Locate every blood parasite and identify its species.
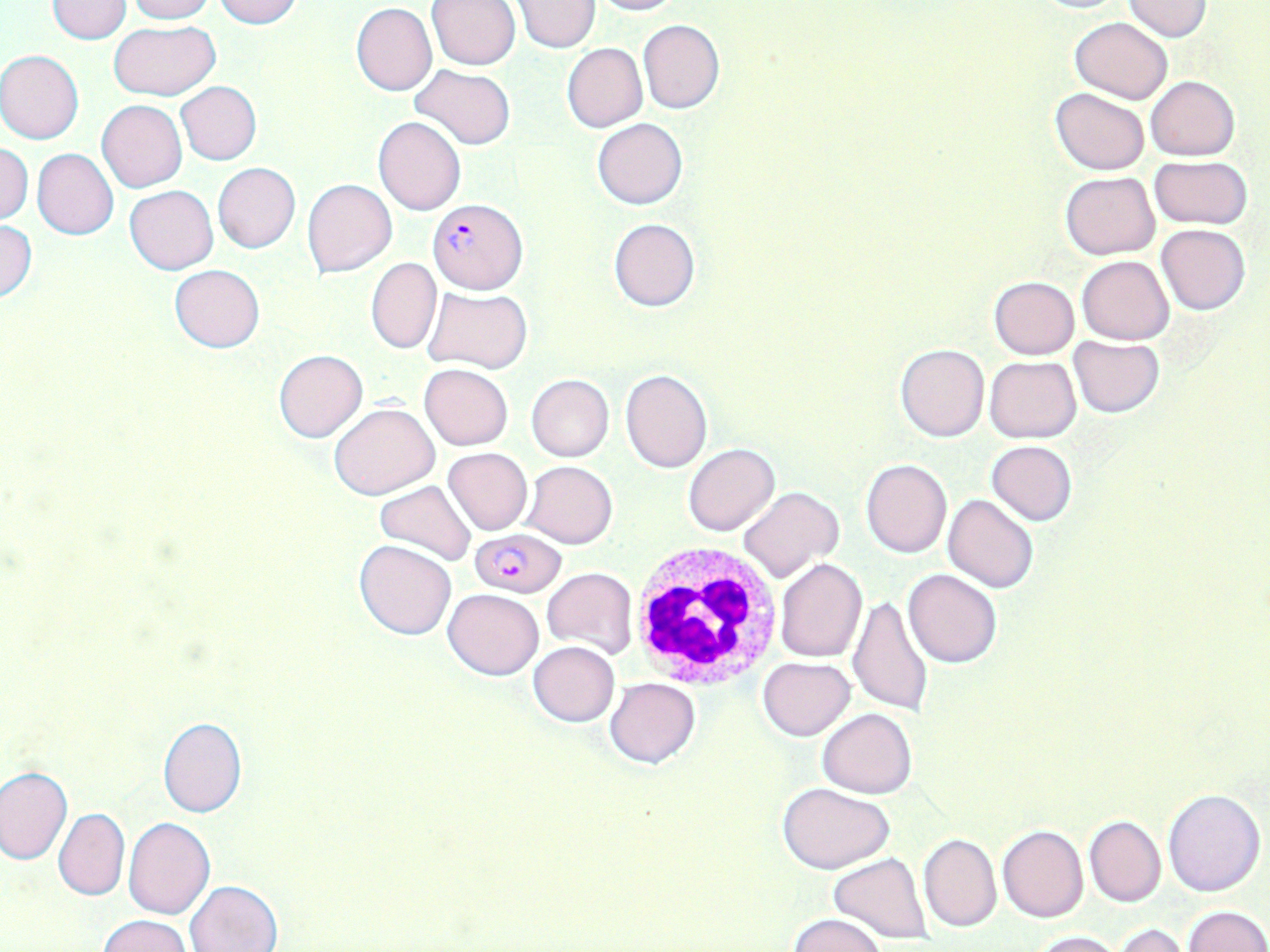

Approximate bounding boxes as named x1/y1/x2/y2 corners in pixels.
Plasmodium falciparum-infected red blood cells: (x1=427, y1=197, x2=528, y2=295), (x1=470, y1=528, x2=566, y2=597).
No Plasmodium ovale, Plasmodium malariae, Plasmodium vivax, Babesia divergens, or Trypanosoma brucei observed.

Summary:
  - White blood cell locations: (x1=628, y1=543, x2=784, y2=690)
  - Uninfected red blood cell locations: (x1=212, y1=0, x2=302, y2=28), (x1=588, y1=0, x2=683, y2=15), (x1=47, y1=1, x2=131, y2=43), (x1=122, y1=1, x2=214, y2=23), (x1=426, y1=1, x2=520, y2=71), (x1=513, y1=1, x2=601, y2=52), (x1=1122, y1=2, x2=1212, y2=41), (x1=351, y1=3, x2=437, y2=95), (x1=1069, y1=17, x2=1173, y2=103), (x1=637, y1=19, x2=724, y2=113), (x1=109, y1=20, x2=222, y2=98), (x1=562, y1=43, x2=648, y2=133), (x1=0, y1=50, x2=84, y2=145), (x1=410, y1=64, x2=516, y2=150), (x1=1146, y1=76, x2=1240, y2=160), (x1=175, y1=81, x2=262, y2=166), (x1=1051, y1=88, x2=1148, y2=175), (x1=98, y1=99, x2=187, y2=192), (x1=373, y1=116, x2=466, y2=215), (x1=592, y1=117, x2=687, y2=210), (x1=1, y1=144, x2=33, y2=223), (x1=32, y1=148, x2=118, y2=240), (x1=1148, y1=155, x2=1252, y2=230), (x1=213, y1=163, x2=300, y2=253), (x1=1060, y1=172, x2=1159, y2=260), (x1=302, y1=177, x2=398, y2=278), (x1=125, y1=185, x2=218, y2=274), (x1=608, y1=218, x2=700, y2=312), (x1=2, y1=221, x2=37, y2=301), (x1=1156, y1=224, x2=1250, y2=314), (x1=1077, y1=256, x2=1173, y2=344), (x1=366, y1=258, x2=442, y2=354), (x1=170, y1=264, x2=264, y2=353), (x1=989, y1=276, x2=1079, y2=358), (x1=423, y1=286, x2=533, y2=373), (x1=1069, y1=335, x2=1163, y2=417), (x1=895, y1=344, x2=989, y2=442), (x1=274, y1=349, x2=367, y2=442), (x1=984, y1=356, x2=1081, y2=442), (x1=419, y1=363, x2=513, y2=450), (x1=620, y1=368, x2=712, y2=472), (x1=526, y1=374, x2=613, y2=462), (x1=330, y1=402, x2=439, y2=499), (x1=986, y1=440, x2=1078, y2=525), (x1=684, y1=443, x2=780, y2=535), (x1=961, y1=444, x2=1067, y2=578), (x1=443, y1=447, x2=533, y2=535), (x1=861, y1=458, x2=952, y2=557), (x1=521, y1=460, x2=617, y2=548), (x1=376, y1=480, x2=478, y2=566), (x1=737, y1=486, x2=842, y2=584), (x1=944, y1=494, x2=1039, y2=594), (x1=355, y1=539, x2=458, y2=641), (x1=774, y1=557, x2=867, y2=662), (x1=542, y1=566, x2=638, y2=660), (x1=903, y1=568, x2=1003, y2=668), (x1=443, y1=588, x2=543, y2=680), (x1=848, y1=596, x2=935, y2=717), (x1=529, y1=641, x2=619, y2=726), (x1=758, y1=657, x2=855, y2=739), (x1=605, y1=678, x2=700, y2=768), (x1=817, y1=708, x2=916, y2=798), (x1=158, y1=717, x2=247, y2=817), (x1=0, y1=765, x2=71, y2=865), (x1=779, y1=783, x2=893, y2=874), (x1=1163, y1=789, x2=1265, y2=897), (x1=53, y1=809, x2=129, y2=901), (x1=1084, y1=815, x2=1165, y2=907), (x1=123, y1=818, x2=215, y2=919), (x1=997, y1=824, x2=1088, y2=923), (x1=918, y1=834, x2=1002, y2=932), (x1=829, y1=854, x2=933, y2=945), (x1=184, y1=880, x2=283, y2=952), (x1=1182, y1=905, x2=1270, y2=952), (x1=788, y1=913, x2=886, y2=952), (x1=99, y1=914, x2=193, y2=952), (x1=1111, y1=924, x2=1191, y2=951), (x1=1031, y1=929, x2=1120, y2=951)
  - Slide-level diagnosis: Plasmodium falciparum
  - Image size: 1270×952 pixels
  - Stain: May-Grünwald-Giemsa
  - Field of view: one of a larger specimen
  - Preparation: thin blood smear
  - Modality: light microscopy
  - Magnification: 1000x